Comment on the morphology of the red blood cells.
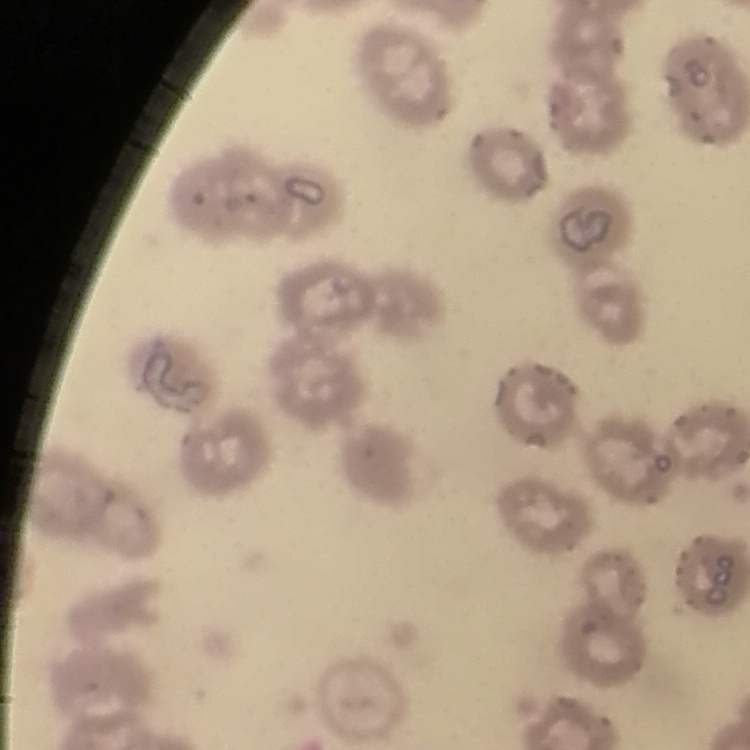
They show no rouleaux formation.

image type = square crop of a larger photomicrograph
stain = Field's or Giemsa
preparation = thin blood film